Locate every malaria parasite.
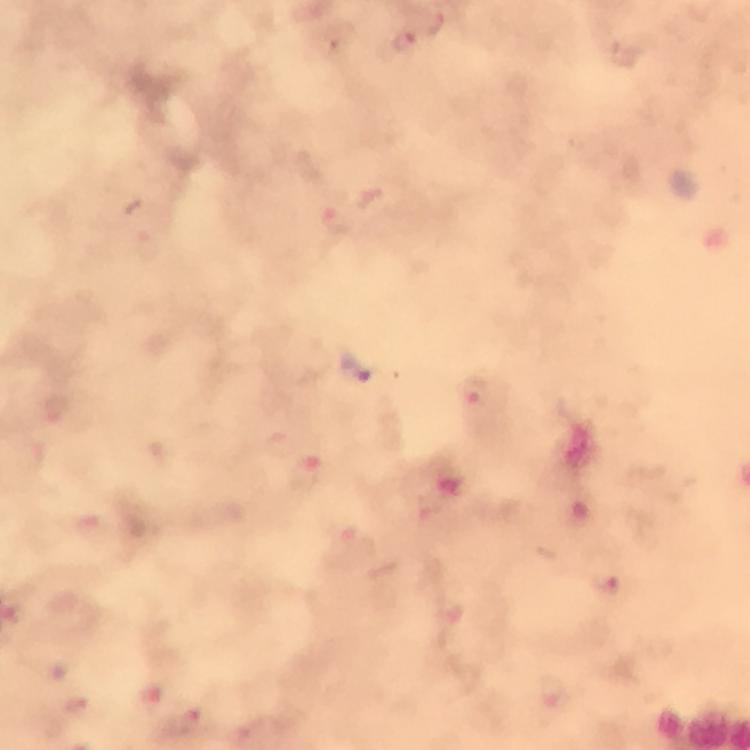
Approximate centers as [x, y] in pixels.
Malaria parasites: [435, 27], [404, 41], [474, 394], [608, 584].

From a malaria diagnostic workup. Image is 750×750 pixels. Thick blood film. Smartphone photograph taken through a microscope. Immersion oil was used. A crop from one field of view. 100x magnification. Giemsa stain.